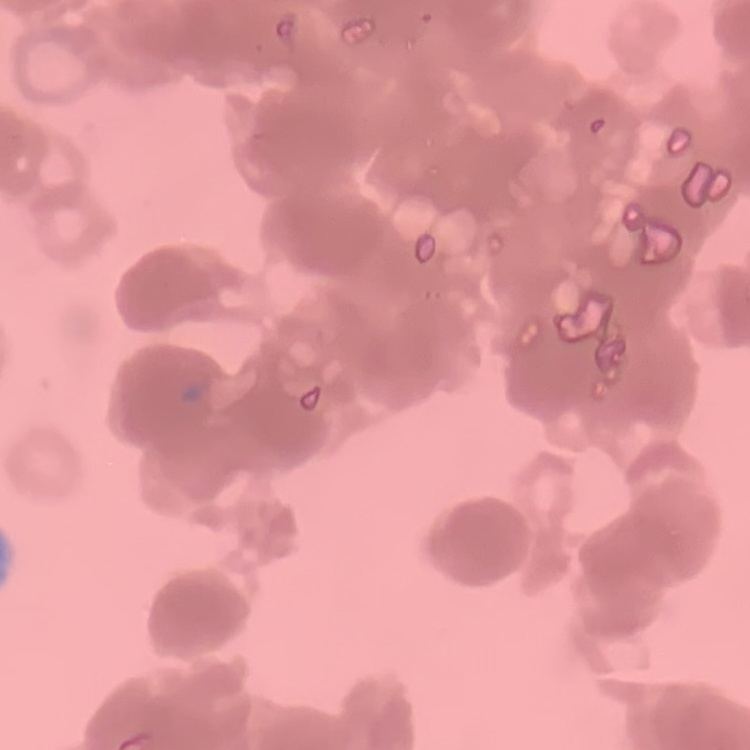
The erythrocytes exhibit rouleaux formation. One tile cut from a larger photomicrograph. Stained with either Field's or Giemsa. Thin blood smear.